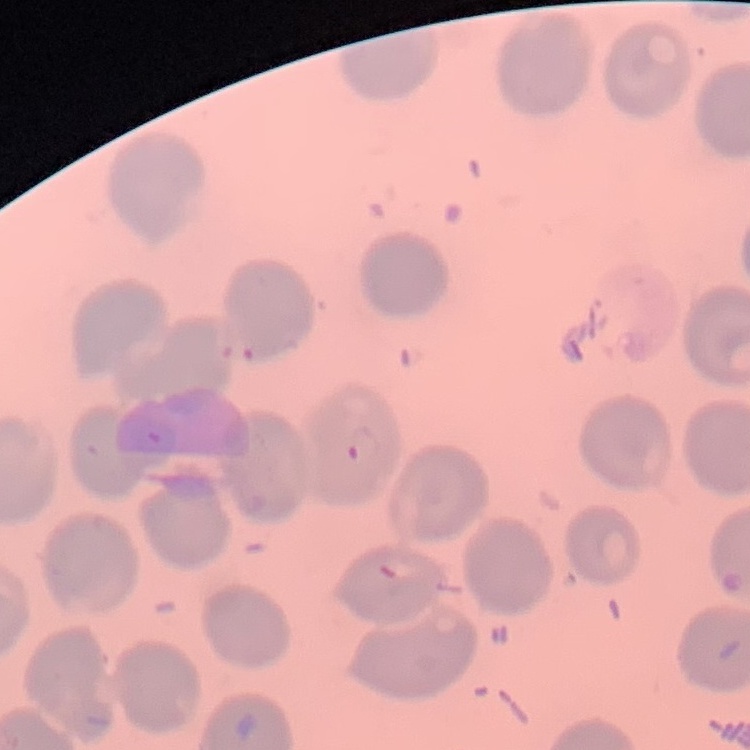
The red blood cells show no rouleaux formation. Thin blood smear. One tile cut from a larger photomicrograph. Stained with either Field's or Giemsa.